Report the malaria status of this cell.
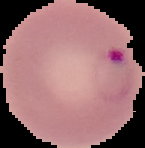
It is parasitized.

Image is 145×148 pixels. From a thin blood film. The area outside the segmented cell region is set to black.